Give the position of every Plasmodium parasite visible.
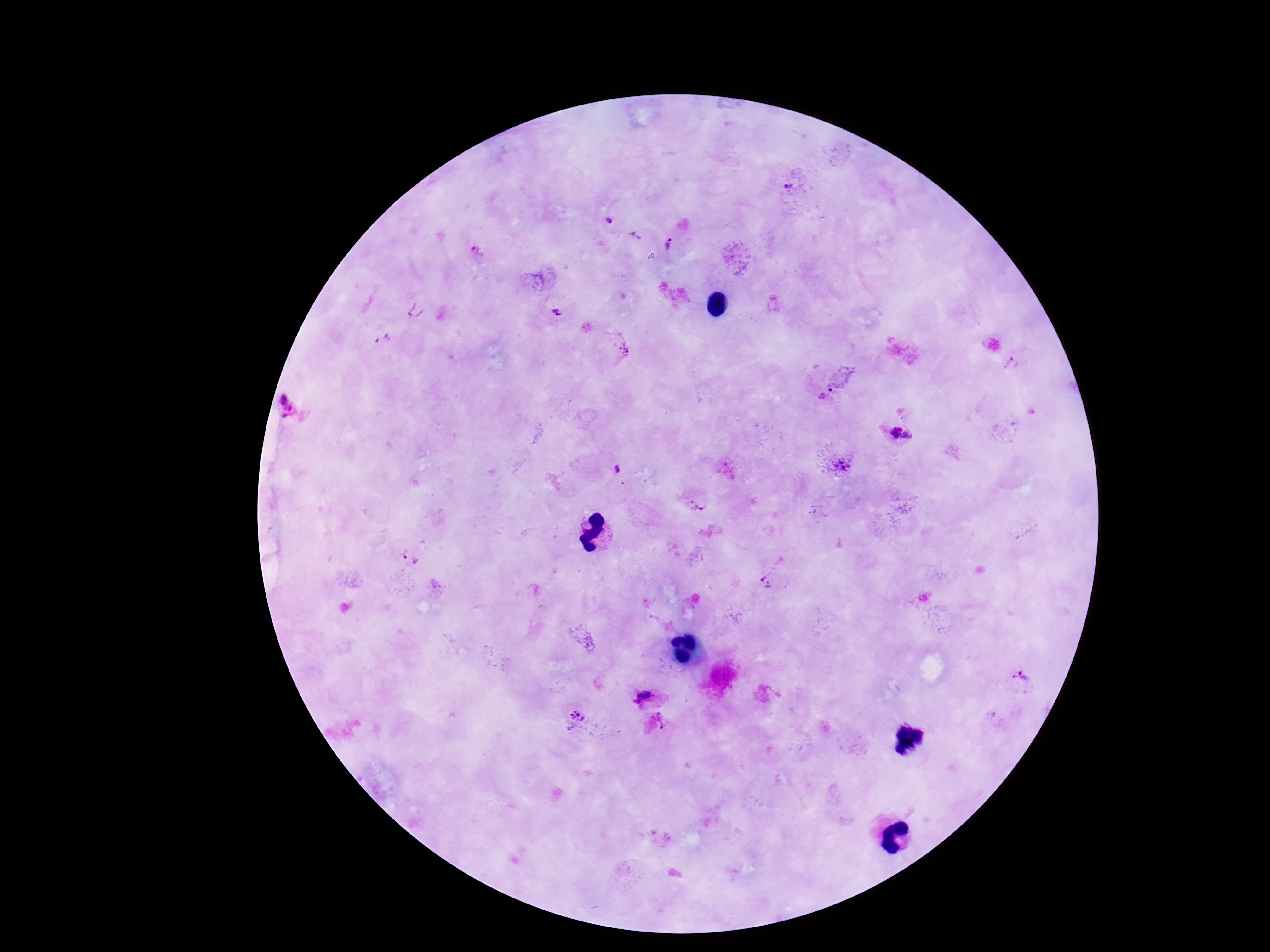

Approximate centers as [x, y] in pixels.
Plasmodium parasites: [791, 187], [609, 221], [635, 236], [670, 244], [478, 252], [415, 310], [558, 313], [383, 338], [623, 348], [1013, 366], [830, 389], [289, 405], [894, 434], [841, 466], [619, 470], [695, 506], [407, 558], [768, 578], [1021, 677], [649, 696], [577, 721], [660, 722].

Summary:
  - Patient malaria status: positive
  - Image size: 1270×952 pixels
  - Capture: smartphone camera through the microscope eyepiece
  - Preparation: thick peripheral-blood smear
  - Stain: Giemsa
  - Magnification: 100x
  - Field of view: single